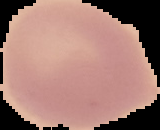

{
  "malaria_status": "uninfected",
  "image_type": "segmented cell region on a black background",
  "preparation": "thin blood film",
  "image_size": "160×130 pixels"
}